Report the malaria status of this cell.
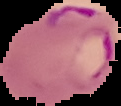
Parasitized.

Image is 121×106 pixels. From a thin blood smear. Cell region segmented out of the field of view; the surrounding area is masked to black.